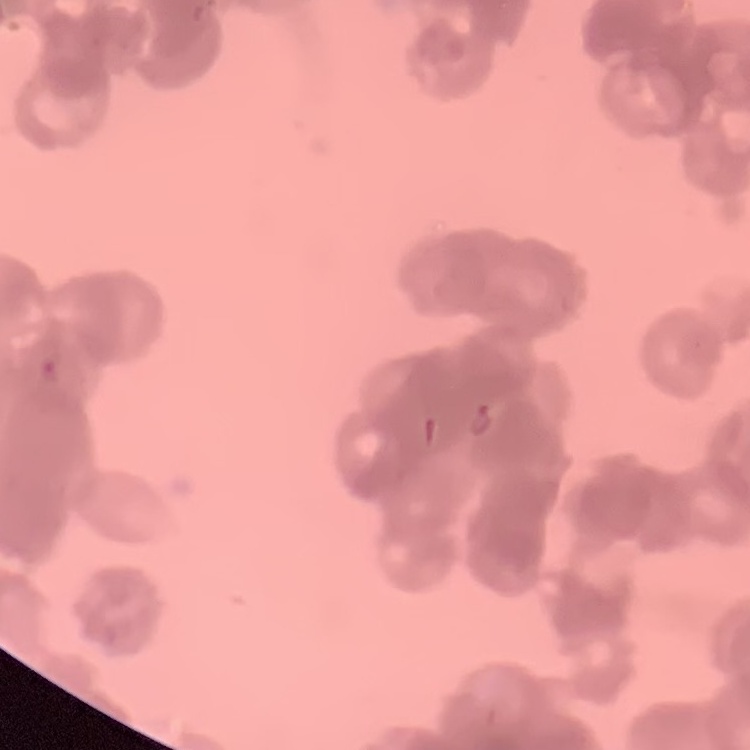
Summary:
  - Red blood cell morphology: rouleaux formation
  - Preparation: thin peripheral smear
  - Stain: Field's or Giemsa
  - Image type: square crop of a larger photomicrograph